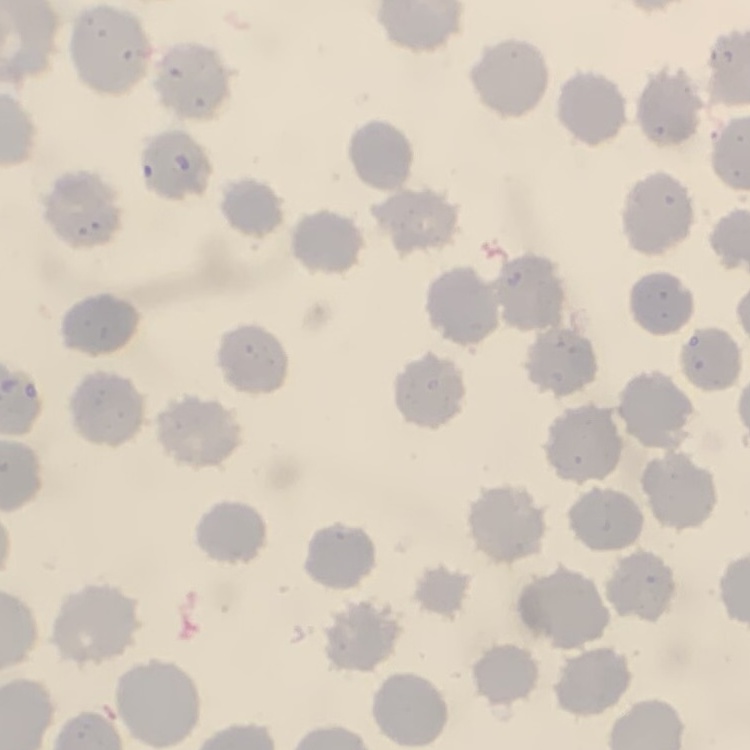

The erythrocytes show no rouleaux formation. Thin blood smear. Field's or Giemsa stain. Square crop of a larger photomicrograph.